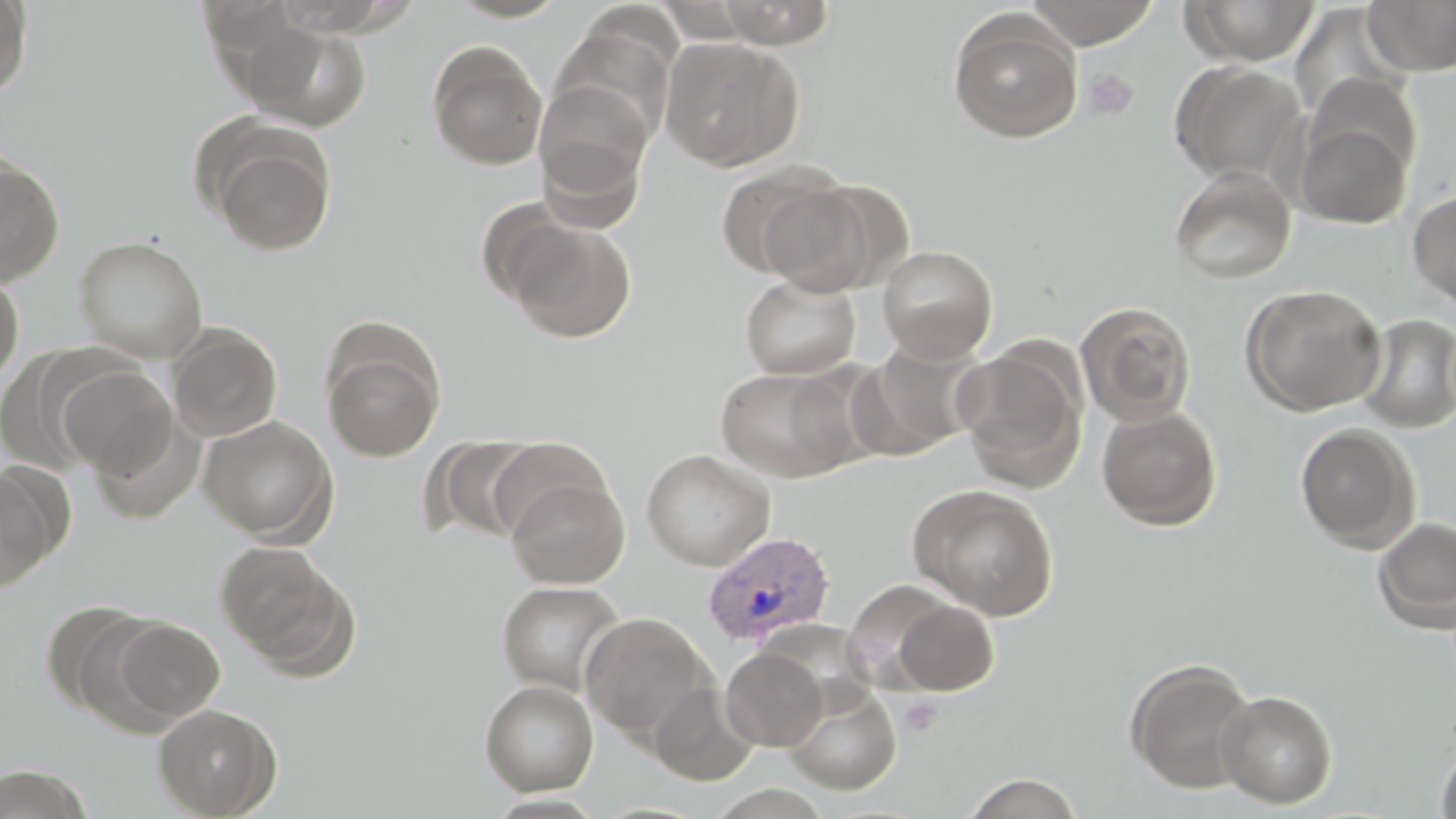

slide-level diagnosis = Plasmodium vivax
image size = 1456×819 pixels
platelet locations = approximate bounding boxes as (x1,y1)-(x2,y2) corner pairs in pixels: (1083,69)-(1139,120), (899,696)-(944,737)
stain = May-Grünwald-Giemsa
magnification = 1000x
modality = light microscopy
field of view = one of a larger specimen
Plasmodium vivax-infected red blood cell locations = approximate bounding boxes as (x1,y1)-(x2,y2) corner pairs in pixels: (702,531)-(836,647)
uninfected red blood cell locations = approximate bounding boxes as (x1,y1)-(x2,y2) corner pairs in pixels: (0,0)-(32,102), (194,0)-(300,62), (269,0)-(407,35), (445,0)-(572,23), (706,0)-(842,48), (1025,0)-(1159,48), (1182,0)-(1320,66), (1362,0)-(1456,76), (1289,4)-(1406,121), (947,11)-(1083,144), (549,20)-(678,147), (240,21)-(372,131), (659,36)-(802,171), (426,41)-(548,171), (1169,61)-(1306,186), (533,81)-(652,217), (1294,111)-(1415,230), (206,127)-(338,255), (0,155)-(64,287), (714,162)-(849,280), (1168,165)-(1297,285), (765,176)-(901,296), (1408,188)-(1456,312), (507,220)-(637,343), (73,235)-(209,363), (878,245)-(998,362), (740,273)-(861,380), (0,274)-(24,390), (1239,283)-(1386,416), (1075,300)-(1197,426), (1355,313)-(1456,434), (167,325)-(283,442), (322,335)-(446,463), (855,337)-(990,459), (952,347)-(1087,491), (58,365)-(176,478), (715,366)-(860,483), (1096,405)-(1223,531), (198,415)-(337,543), (1295,423)-(1420,552), (427,435)-(546,544), (491,436)-(613,544), (640,448)-(775,571), (0,468)-(59,591), (505,473)-(629,589), (907,484)-(1060,620), (1372,516)-(1456,633), (214,539)-(358,675), (496,581)-(626,696), (40,598)-(163,721), (890,600)-(1000,695), (580,612)-(714,741), (110,618)-(224,725), (720,647)-(828,751), (1124,658)-(1258,795), (479,679)-(599,796), (782,679)-(902,795), (647,682)-(761,785), (1215,689)-(1338,809), (153,703)-(282,818), (1435,743)-(1456,819), (0,764)-(94,818), (962,772)-(1084,818)
preparation = thin blood smear